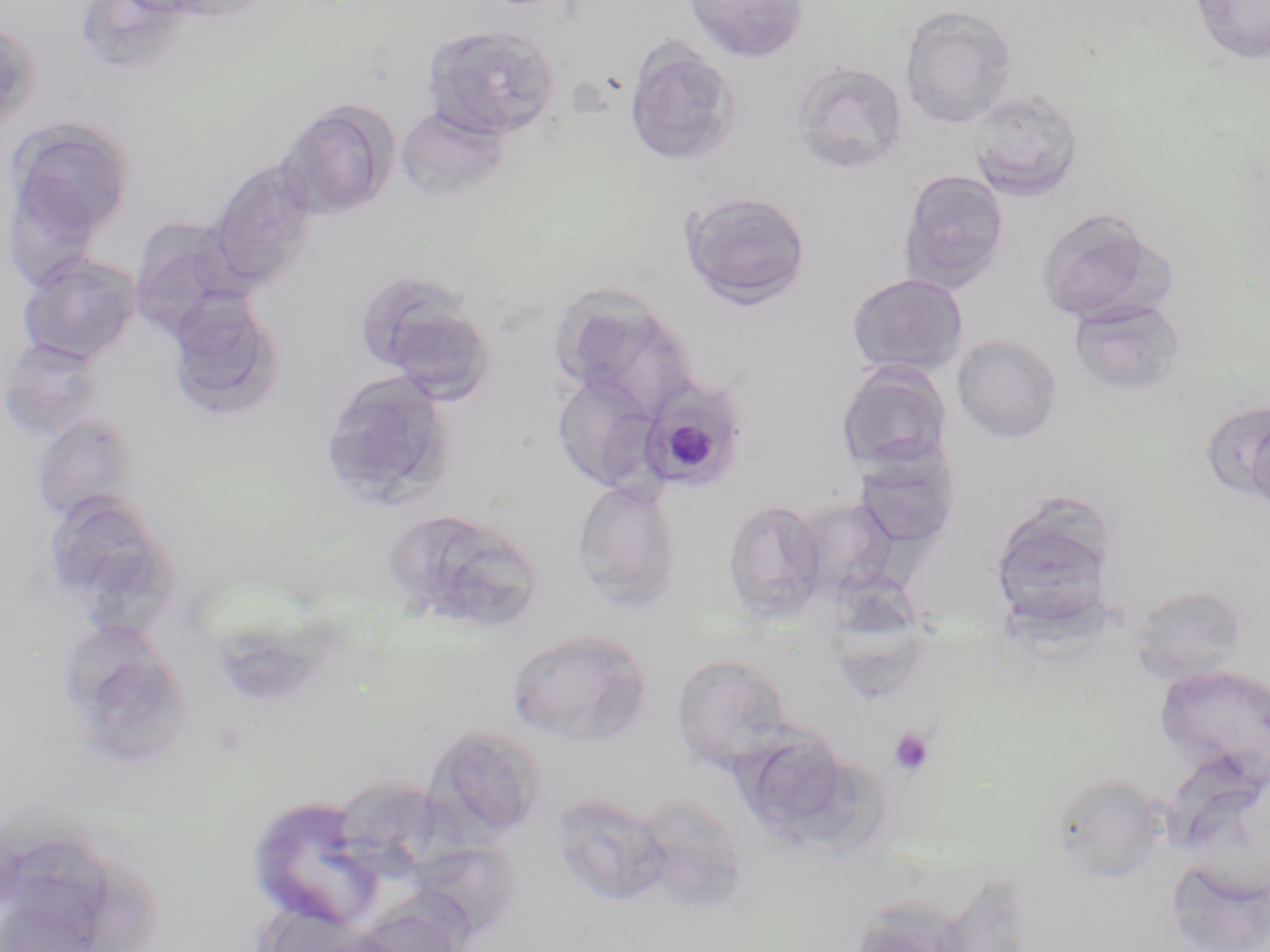

Approximate bounding boxes as (x1,y1)-(x2,y2) corner pairs in pixels. Uninfected red blood cell locations: (150,0)-(275,24), (684,0)-(809,63), (1189,0)-(1270,65), (901,5)-(1018,127), (0,20)-(41,135), (422,24)-(560,140), (622,40)-(741,168), (791,60)-(908,175), (969,89)-(1084,202), (277,100)-(399,221), (396,104)-(509,202), (6,118)-(135,255), (207,159)-(319,291), (897,169)-(1011,293), (679,189)-(812,310), (1035,208)-(1174,326), (128,217)-(245,338), (17,254)-(141,365), (355,270)-(496,399), (845,272)-(970,378), (165,291)-(285,422), (553,291)-(699,419), (1068,299)-(1188,398), (952,334)-(1063,443), (1,336)-(105,442), (835,362)-(953,474), (319,370)-(456,509), (552,372)-(660,492), (1202,399)-(1270,507), (1245,410)-(1270,515), (31,413)-(141,524), (852,448)-(960,551), (572,480)-(684,613), (40,493)-(179,628), (793,497)-(901,600), (724,499)-(828,622), (989,503)-(1119,631), (385,507)-(545,635), (830,564)-(930,700), (1130,585)-(1249,684), (59,625)-(196,768), (507,629)-(653,746), (672,653)-(793,774), (1154,662)-(1270,787), (423,725)-(548,844), (738,726)-(845,832), (785,757)-(904,858), (1050,773)-(1166,882), (342,777)-(478,877), (246,793)-(387,932), (549,793)-(672,907), (630,794)-(751,912), (414,837)-(526,932), (1166,857)-(1270,952), (932,871)-(1034,952), (350,900)-(471,952), (846,904)-(970,952). Platelet locations: (887,726)-(936,776). Plasmodium malariae-infected red blood cell locations: (644,385)-(749,488). Slide-level diagnosis: Plasmodium malariae. One field of a larger specimen. Image is 1270×952 pixels. May-Grünwald-Giemsa-stained preparation. 1000x magnification. Optical microscopy. Thin blood film.